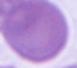
{
  "modality": "micrograph",
  "identification": "red blood cell",
  "magnification": "1000x"
}